Comment on the morphology of the red blood cells.
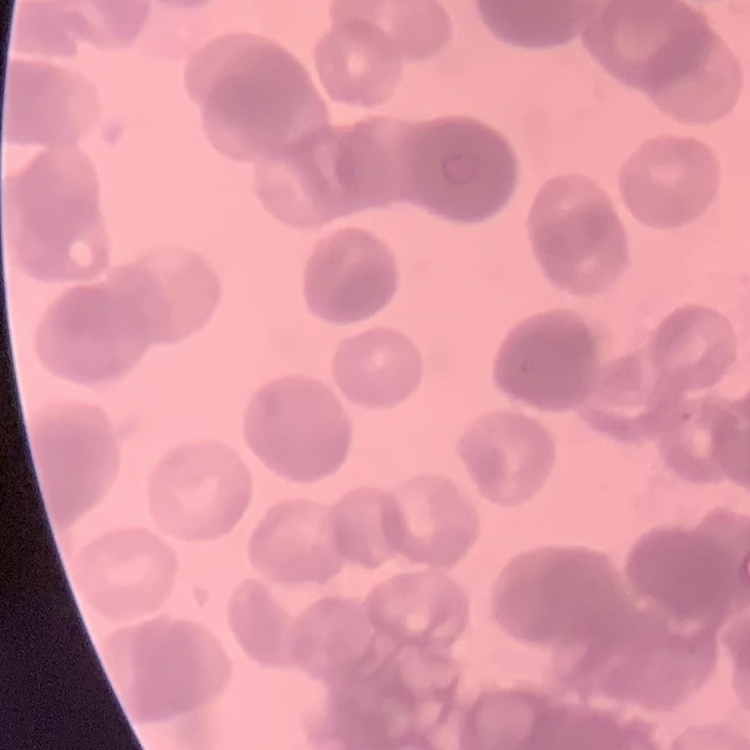

They show rouleaux formation.

Summary:
  - Image type: square crop of a larger photomicrograph
  - Preparation: thin blood film
  - Stain: Field's or Giemsa